Report the malaria status of this cell.
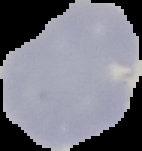
It is uninfected.

image type = segmented cell region on a black background
preparation = thin blood smear
image size = 142×151 pixels